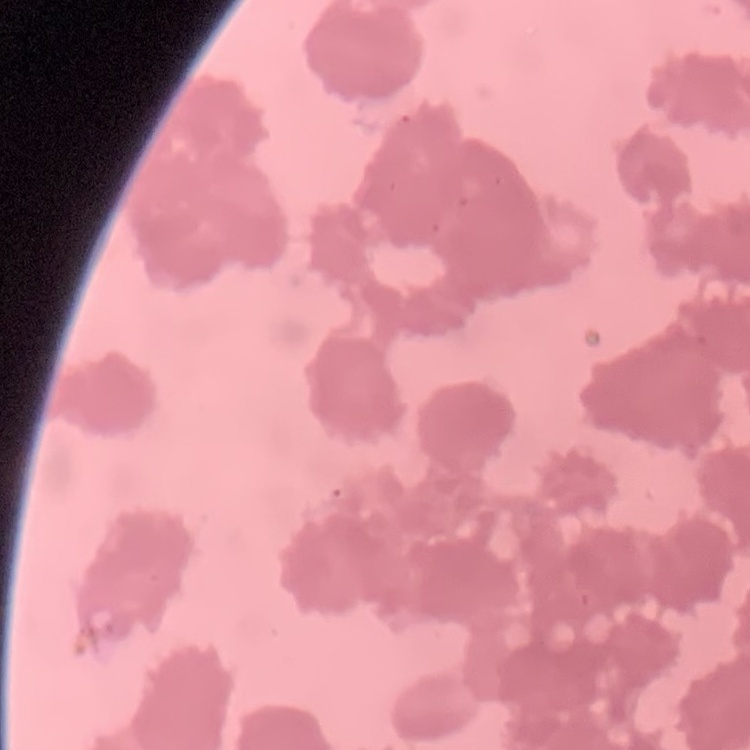

Summary:
  - Erythrocyte morphology: rouleaux formation
  - Preparation: thin blood smear
  - Image type: square crop of a larger photomicrograph
  - Stain: Field's or Giemsa